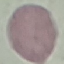

Result: no malaria parasites detected. Automatically extracted cell patch, resized to 64 × 64 pixels. Photographed with a smartphone camera at the microscope eyepiece. Giemsa stain. Thin smear of blood.